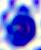
identification: leukocyte
modality: micrograph
magnification: 400x